Locate every Plasmodium parasite.
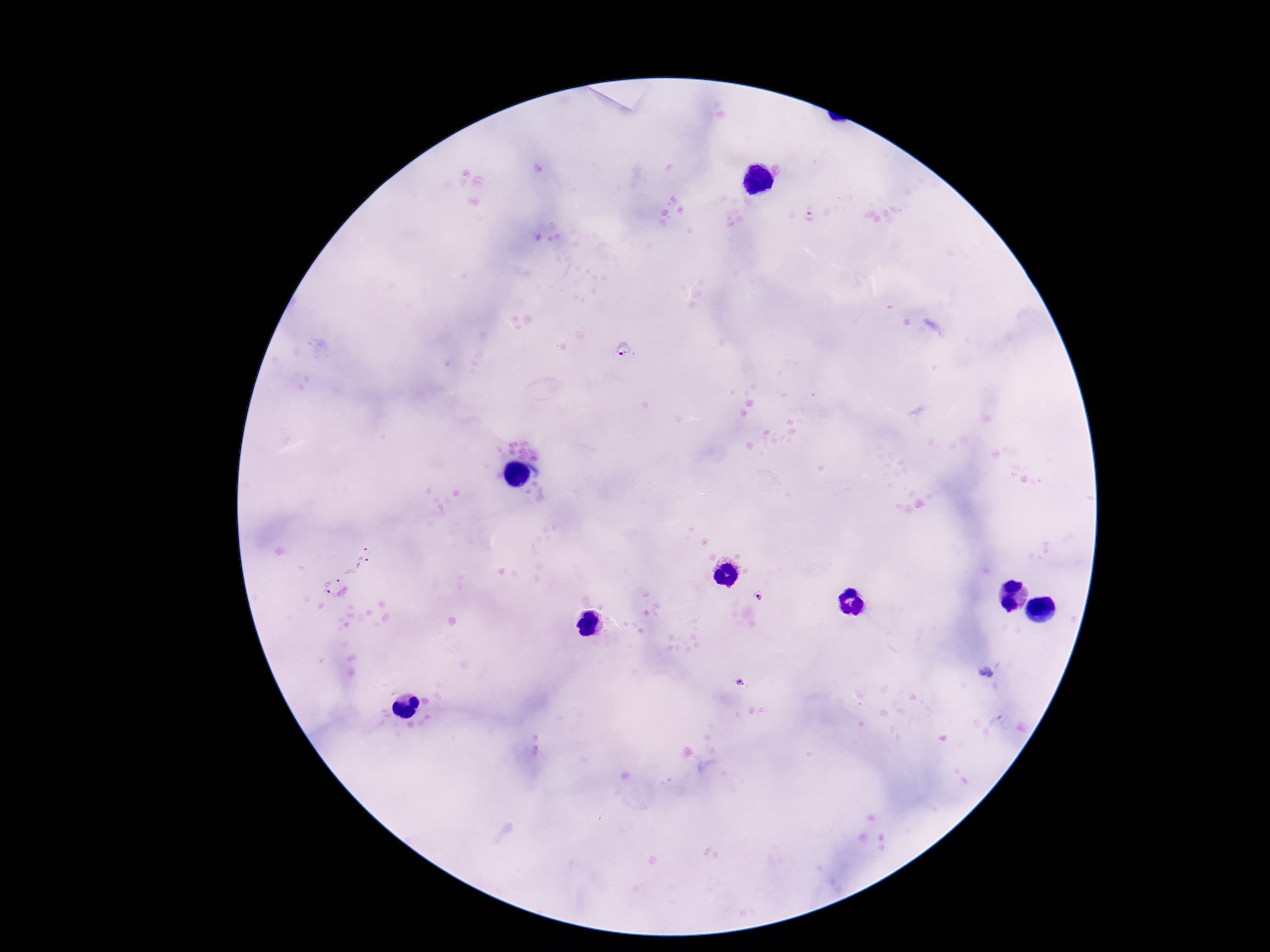
Approximate centers as (x, y) in pixels.
Plasmodium parasites: (808, 218), (628, 351), (360, 551), (365, 567), (345, 578), (325, 587), (758, 596), (987, 673), (741, 683).

field_of_view: one from this slide
magnification: 100x
patient_malaria_status: positive
image_size: 1270×952 pixels
stain: Giemsa
preparation: thick blood smear
capture: smartphone camera through the microscope eyepiece